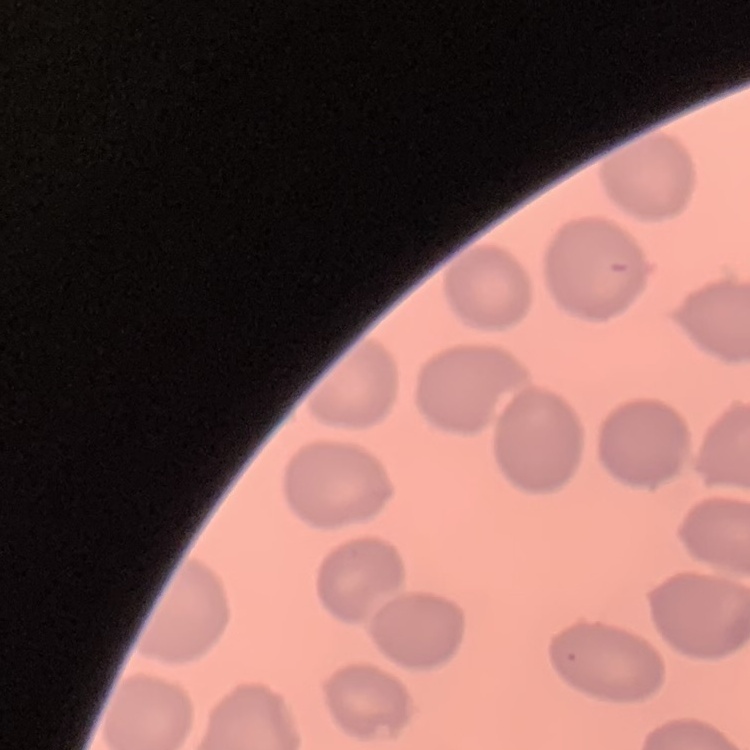
erythrocyte morphology = no rouleaux formation
image type = one tile cut from a larger photomicrograph
stain = Field's or Giemsa
preparation = thin peripheral smear